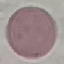

Result: negative for malaria parasites. Thin blood film. Photographed with a smartphone camera at the microscope eyepiece. Automatically extracted cell patch, resized to 64 × 64 pixels. Giemsa stain.